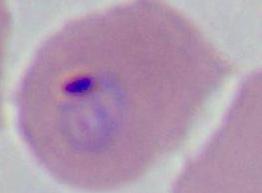
magnification = 400x or 1000x
modality = micrograph
identification = Plasmodium